Identify the parasite.
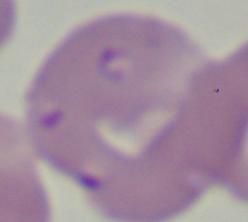

Babesia.

1000x magnification. Photomicrograph.